Classify this cell by malaria status.
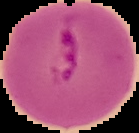

Parasitized.

Summary:
  - Image size: 139×133 pixels
  - Preparation: thin blood smear
  - Image type: segmented cell region on a black background